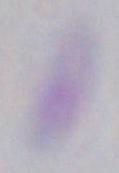 Photomicrograph. Toxoplasma gondii is shown. 1000x magnification.